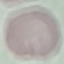
malaria status = uninfected
stain = Giemsa
preparation = thin blood film
image type = cell patch, automatically extracted from a larger field of view and resized to 64 × 64 pixels
capture = smartphone through the microscope eyepiece